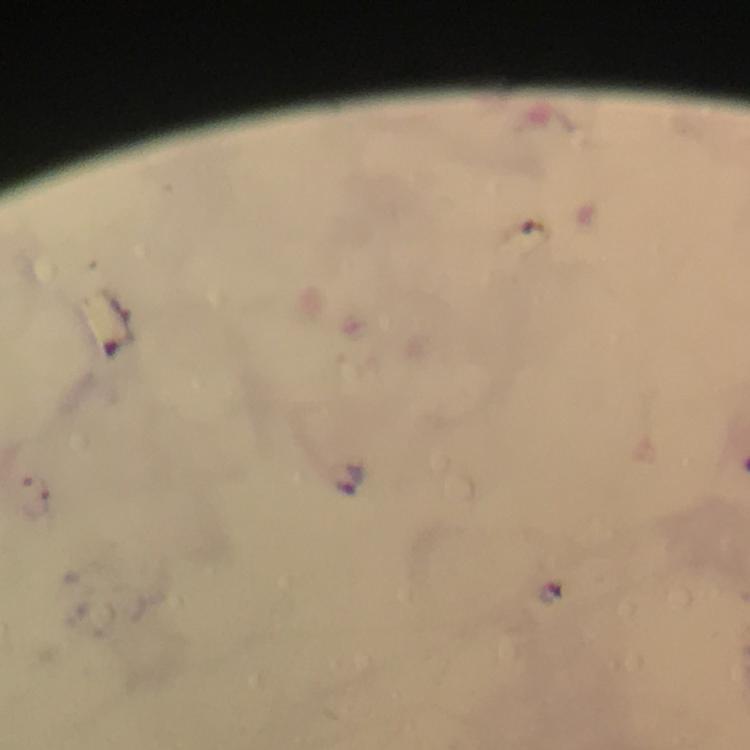

Approximate object centers, in pixels from the top-left corner. Malaria parasite locations: (x=351, y=479). From a diagnostic examination for malaria. Immersion oil was used. Thick blood smear. Cropped region of a single field of view. Giemsa-stained preparation. Photographed with a smartphone mounted on the microscope. Image is 750×750 pixels. At 100x magnification.